Point out each leukocyte.
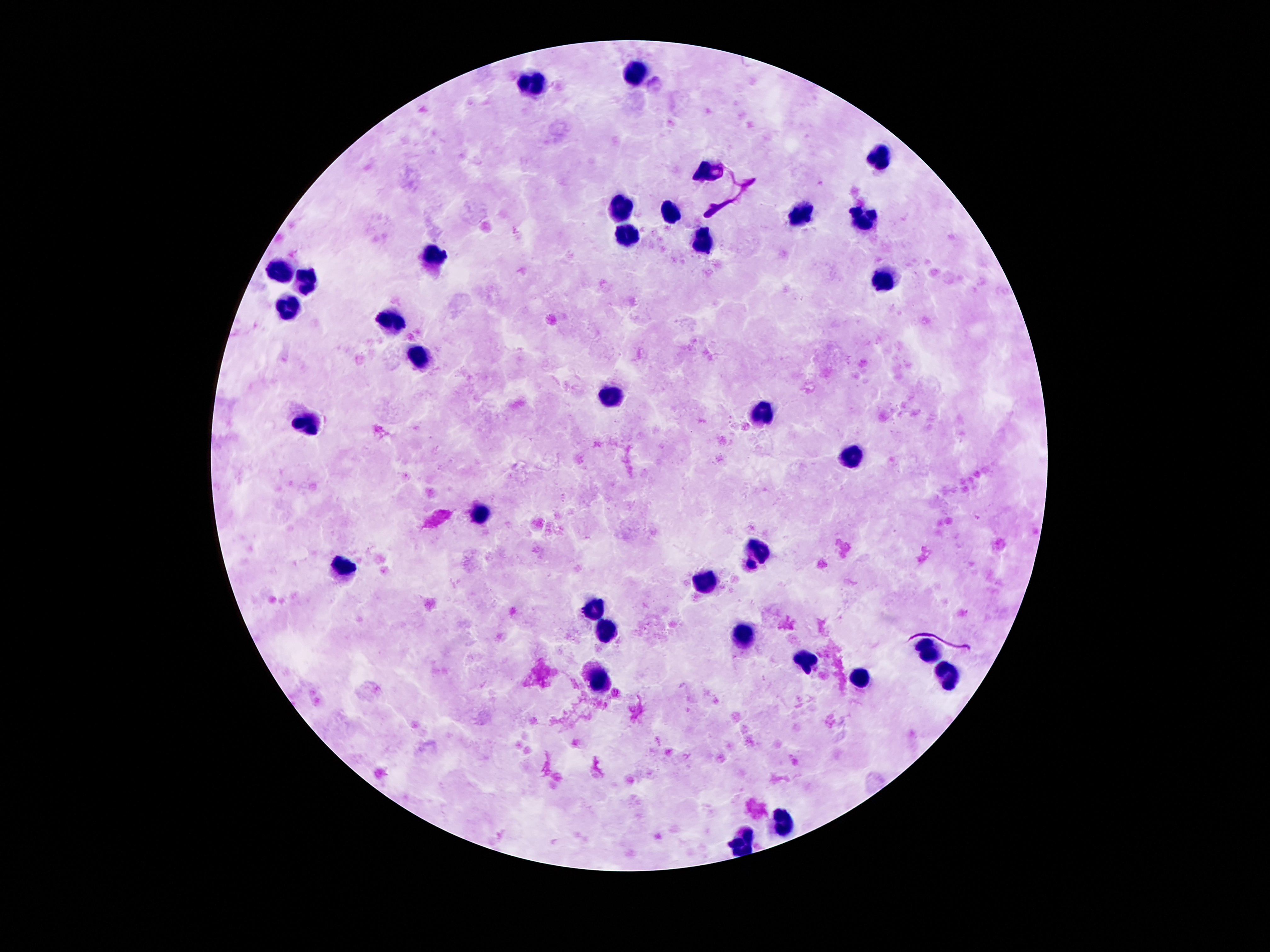

Approximate object centers, in pixels from the top-left corner.
Leukocytes: (x=637, y=73), (x=528, y=82), (x=880, y=155), (x=708, y=170), (x=623, y=203), (x=670, y=210), (x=803, y=212), (x=864, y=217), (x=628, y=237), (x=703, y=246), (x=436, y=256), (x=279, y=268), (x=305, y=279), (x=882, y=281), (x=290, y=310), (x=393, y=321), (x=416, y=356), (x=608, y=396), (x=761, y=414), (x=312, y=423), (x=851, y=456), (x=478, y=513), (x=763, y=551), (x=343, y=568), (x=707, y=582), (x=593, y=610), (x=608, y=626), (x=743, y=637), (x=929, y=652), (x=803, y=662), (x=597, y=675), (x=950, y=675), (x=860, y=677), (x=785, y=819), (x=740, y=843).

Patient malaria status: negative. Smartphone photograph taken through the microscope eyepiece. Thick peripheral-blood smear. Single field of view. Giemsa-stained preparation. Image is 1270×952 pixels. 100x magnification.